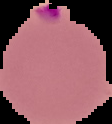

Result: malaria parasites identified. The area outside the segmented cell region is set to black. From a thin blood smear. Image is 112×124 pixels.